Give the position of every Plasmodium falciparum parasite, noting its life-cycle stage.
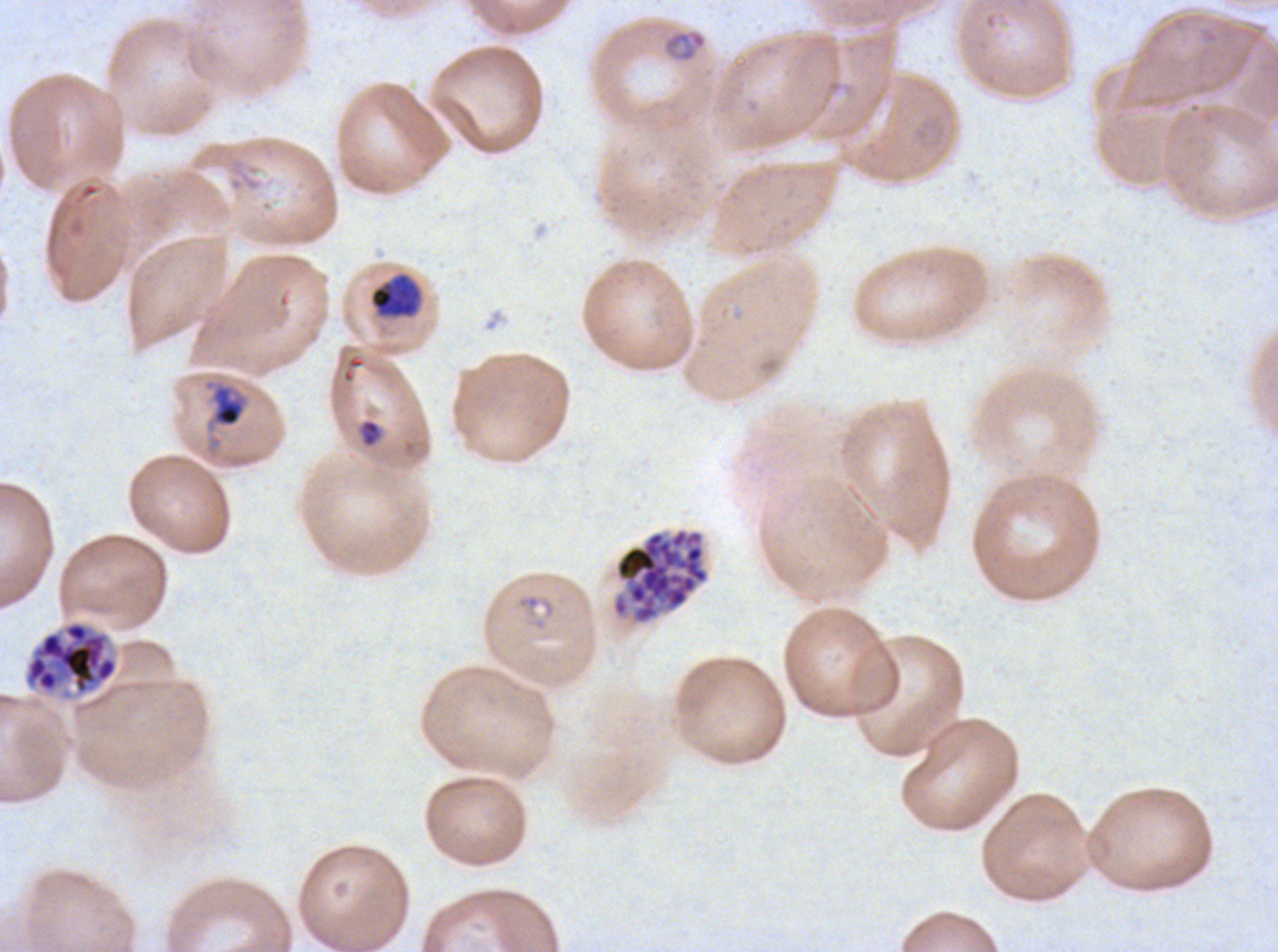

Approximate bounding boxes as {x1, y1, x2, y2} in pixels.
Rings: {663, 29, 707, 63}, {514, 592, 558, 632}.
Late-ring/early-trophozoite forms: {213, 385, 245, 427}, {358, 418, 383, 448}.
Early schizonts: {369, 272, 423, 319}.
Late schizonts: {22, 619, 119, 702}.
Segmenters: {611, 527, 709, 625}.
No mid trophozoites, late trophozoites, or gametocytes observed.

Summary:
  - Specimen: Plasmodium falciparum from a patient in The Gambia, cultured ex vivo for 24 to 48 hours
  - Life-cycle stages observed: ring, late-ring/early-trophozoite, early schizont, late schizont, segmenter
  - Stain: Giemsa
  - Image size: 1278×952 pixels
  - Preparation: thin blood smear
  - Field of view: sub-image separated from a larger composite